Find the red blood cells and label each as P. falciparum-infected, uninfected, or of indeterminate infection status.
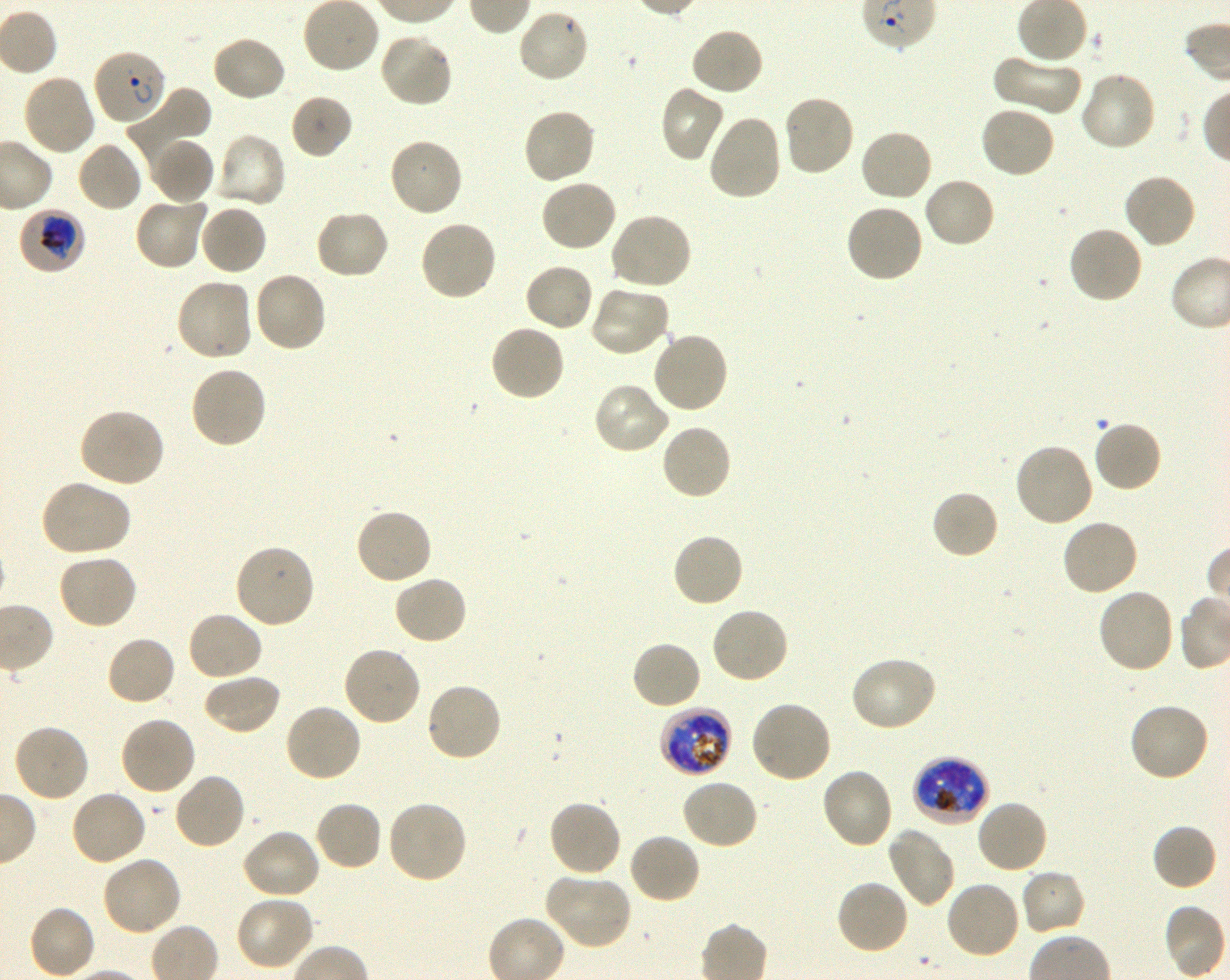
Approximate bounding boxes as [x1, y1, x2, y2] in pixels. Not every red blood cell is marked. A life-cycle stage — or a range of stages, where the recorded stages span more than one — follows each staged infected red blood cell.
Infected red blood cells: [93, 47, 167, 125] ring; [17, 207, 86, 275] trophozoite; [659, 705, 733, 777] late trophozoite to late schizont; [911, 756, 989, 827] late trophozoite to early schizont.
Uninfected red blood cells: [517, 8, 591, 84], [690, 27, 765, 97], [378, 33, 454, 108], [211, 35, 286, 103], [992, 52, 1082, 116], [1078, 71, 1157, 153], [21, 72, 96, 156], [660, 84, 725, 163], [128, 88, 212, 165], [289, 93, 353, 160], [781, 93, 855, 178], [978, 105, 1056, 179], [522, 107, 597, 186], [706, 113, 783, 202], [859, 127, 935, 203], [213, 132, 287, 211], [150, 136, 215, 205], [387, 138, 464, 219], [76, 141, 143, 214], [1122, 173, 1198, 249], [922, 175, 997, 249], [540, 178, 619, 253], [134, 194, 209, 271], [198, 203, 268, 276], [844, 203, 925, 283], [313, 209, 391, 280], [608, 211, 692, 291], [417, 218, 497, 301], [1067, 225, 1144, 305], [523, 262, 594, 333], [252, 270, 327, 354], [174, 276, 253, 362], [590, 283, 671, 358], [489, 323, 566, 402], [651, 331, 730, 414], [188, 364, 268, 450], [592, 381, 672, 455], [76, 406, 165, 488], [1092, 419, 1163, 493], [659, 423, 733, 502], [1013, 441, 1095, 528], [38, 480, 131, 558], [931, 489, 1000, 560], [354, 506, 434, 586], [1061, 517, 1140, 596], [671, 532, 746, 609], [233, 543, 316, 629], [56, 553, 139, 630], [392, 575, 469, 646], [1096, 587, 1176, 675], [709, 606, 789, 685], [186, 610, 264, 682], [105, 635, 177, 706], [630, 639, 703, 710], [342, 645, 422, 728], [849, 655, 938, 733], [202, 672, 282, 736], [425, 681, 503, 763], [749, 699, 833, 785], [1128, 701, 1211, 783], [283, 702, 363, 783], [118, 715, 197, 796], [12, 723, 90, 803], [821, 767, 896, 849], [173, 772, 247, 850], [680, 778, 760, 851], [69, 788, 148, 866], [547, 798, 622, 878], [975, 798, 1049, 875], [386, 799, 468, 885], [314, 800, 383, 871], [1151, 824, 1217, 892], [886, 826, 956, 908], [240, 827, 321, 900], [627, 832, 702, 904], [100, 856, 183, 938], [1019, 867, 1086, 936], [543, 873, 632, 950], [834, 879, 911, 956], [944, 879, 1022, 961], [234, 896, 315, 972], [28, 904, 97, 979].
No red blood cells of indeterminate infection status observed.

Summary:
  - Donor blood group: O+
  - Life-cycle stages observed: ring, trophozoite
  - Preparation: thin blood smear
  - Stain: Giemsa
  - Culture: in-vitro P. falciparum strain 3D7, shaking
  - Objective: 100x, oil immersion, numerical aperture 1.30
  - Field of view: single
  - Image size: 1230×980 pixels